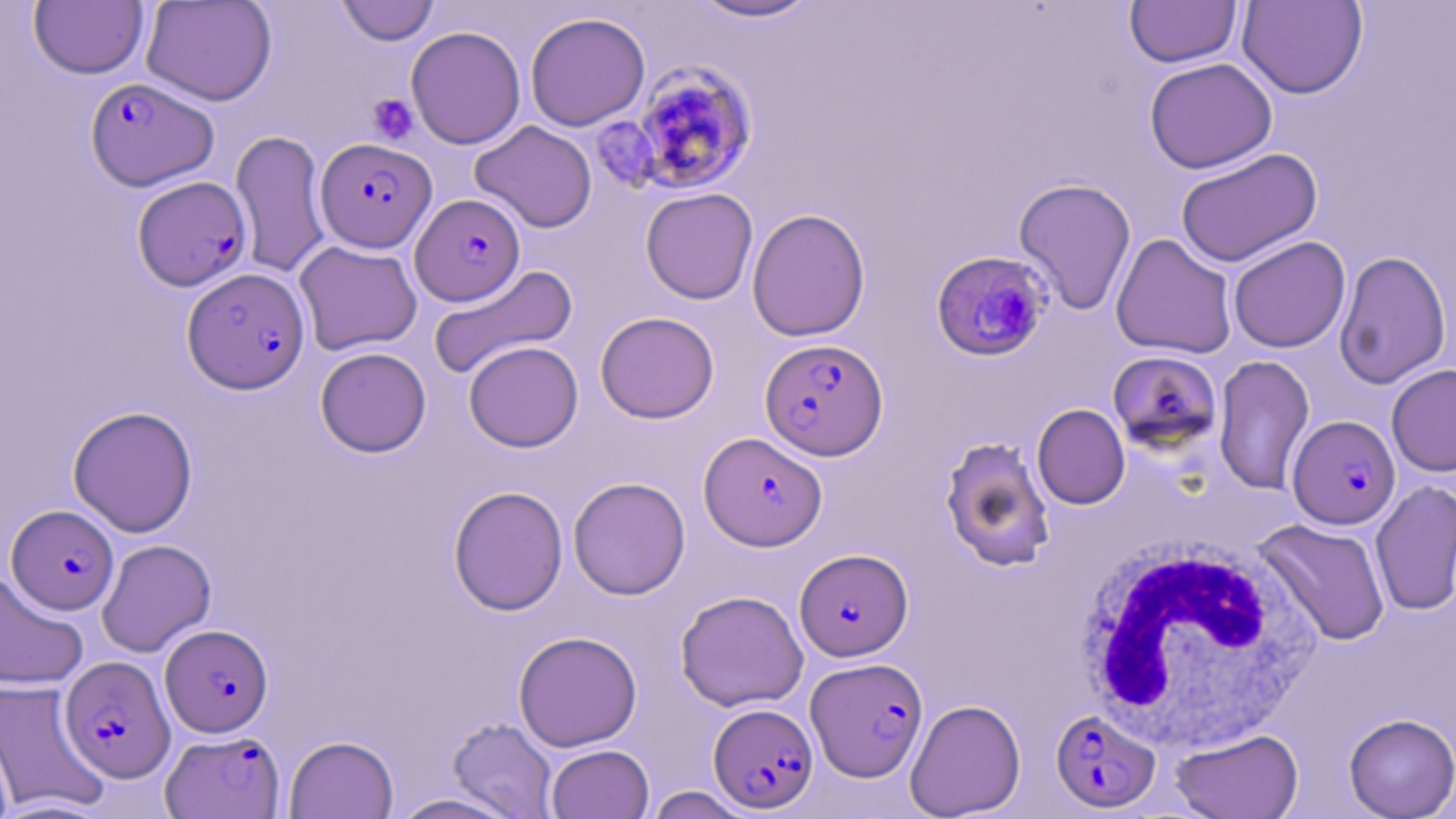

Approximate bounding boxes as (x1,y1)-(x2,y2) corner pairs in pixels. Platelet locations: (367,93)-(418,145). White blood cell locations: (1076,539)-(1324,754). Uninfected red blood cell locations: (140,0)-(277,106), (687,0)-(822,23), (1237,0)-(1368,99), (29,1)-(148,79), (335,1)-(440,46), (1124,1)-(1242,68), (524,12)-(650,131), (406,25)-(526,150), (1144,57)-(1277,174), (470,120)-(597,233), (230,129)-(332,279), (1175,147)-(1322,267), (1013,178)-(1137,315), (640,187)-(758,304), (746,208)-(871,342), (1111,233)-(1237,359), (1228,236)-(1350,353), (294,240)-(422,355), (1333,249)-(1451,389), (428,265)-(578,381), (595,311)-(719,424), (463,340)-(584,452), (315,347)-(431,457), (1212,355)-(1315,496), (1386,364)-(1456,476), (1032,404)-(1130,509), (68,405)-(198,537), (940,436)-(1055,572), (568,477)-(690,599), (1370,480)-(1456,617), (448,485)-(568,615), (1254,518)-(1392,646), (96,539)-(216,657), (0,569)-(89,692), (675,590)-(809,712), (513,631)-(642,751), (0,679)-(108,815), (905,698)-(1026,818), (1343,713)-(1456,818), (447,717)-(559,818), (0,719)-(18,819), (1170,728)-(1303,819), (284,735)-(398,818), (546,744)-(654,819), (643,786)-(755,818), (388,793)-(525,819). Plasmodium falciparum-infected red blood cell locations: (629,61)-(759,197), (85,77)-(219,191), (316,137)-(436,252), (133,175)-(252,292), (411,194)-(525,305), (931,250)-(1053,361), (183,267)-(310,393), (760,338)-(888,460), (1107,350)-(1223,454), (1287,415)-(1400,529), (699,432)-(827,551), (7,505)-(119,614), (794,548)-(913,661), (160,624)-(272,737), (60,656)-(175,783), (806,657)-(928,782), (708,703)-(818,813), (1051,708)-(1161,813), (161,729)-(285,818). Slide-level diagnosis: Plasmodium falciparum. Optical microscopy. May-Grünwald-Giemsa-stained preparation. Single field of view. Thin blood smear. 1000x magnification. Image is 1456×819 pixels.